Outline each uninfected red blood cell.
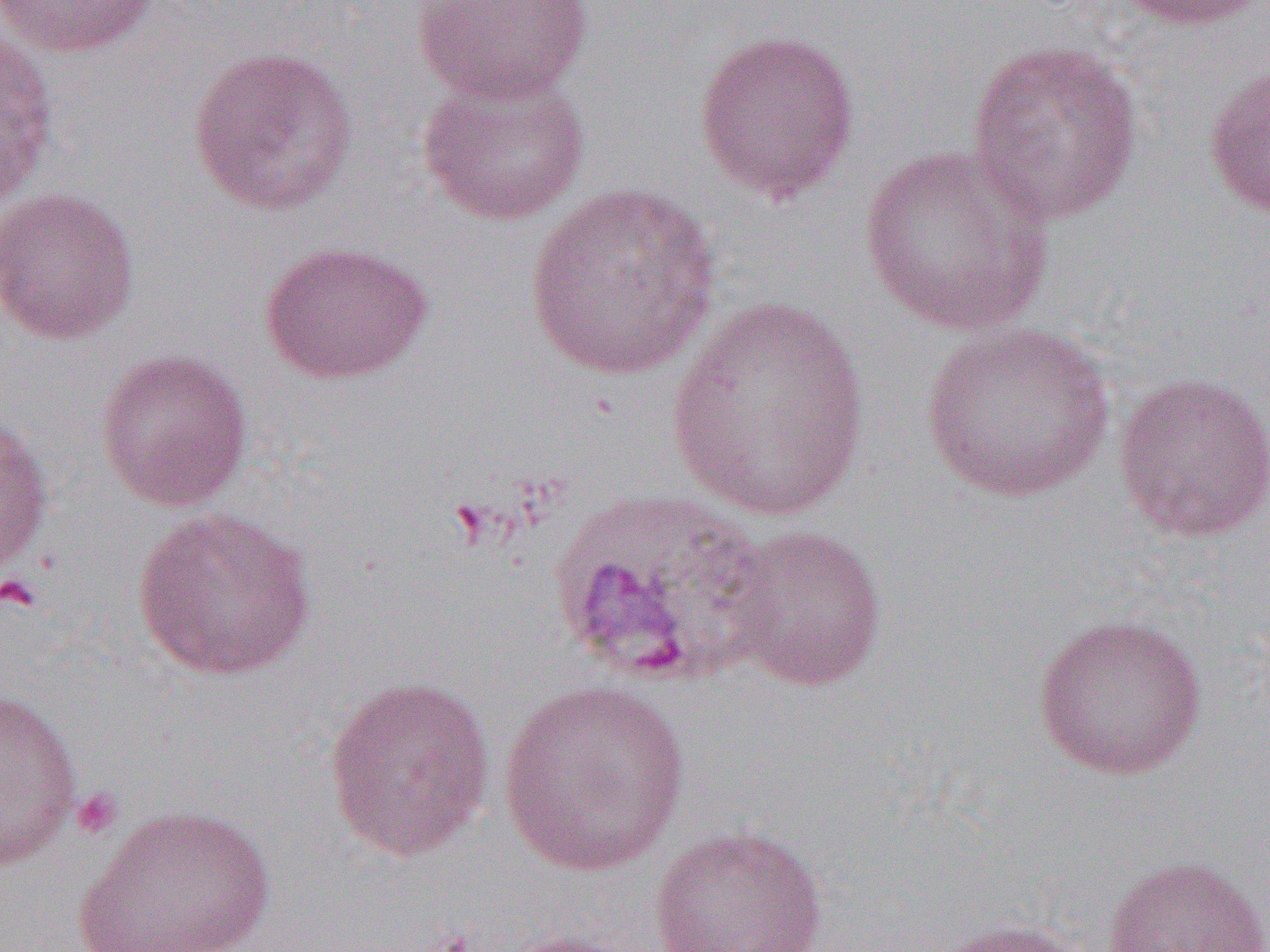

Approximate bounding boxes as (x1,y1)-(x2,y2) corner pairs in pixels.
Uninfected red blood cells: (0,0)-(164,59), (409,0)-(593,103), (1112,0)-(1269,31), (0,24)-(59,211), (692,28)-(861,205), (965,38)-(1143,225), (187,45)-(359,217), (1203,57)-(1270,223), (415,65)-(591,226), (857,143)-(1059,336), (523,181)-(723,380), (0,187)-(141,345), (258,239)-(433,385), (665,296)-(874,523), (920,322)-(1116,504), (93,347)-(254,512), (1112,371)-(1270,543), (0,409)-(55,583), (131,506)-(318,682), (723,525)-(888,692), (1032,612)-(1208,781), (323,675)-(496,863), (497,679)-(692,876), (0,686)-(83,872), (71,803)-(278,952), (647,825)-(829,952), (1102,855)-(1269,952), (928,917)-(1087,952), (494,930)-(638,952).

Summary:
  - Platelet locations: (0,573)-(42,613), (70,787)-(124,841)
  - Slide-level diagnosis: Plasmodium vivax
  - Field of view: one of a larger specimen
  - Image size: 1270×952 pixels
  - Modality: light microscopy
  - Preparation: thin blood film
  - Magnification: 1000x